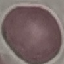

Malaria status: uninfected. Thin blood smear. Cell patch, automatically extracted from a larger field of view and resized to 64 × 64 pixels. Photographed with a smartphone camera at the microscope eyepiece. Giemsa-stained preparation.